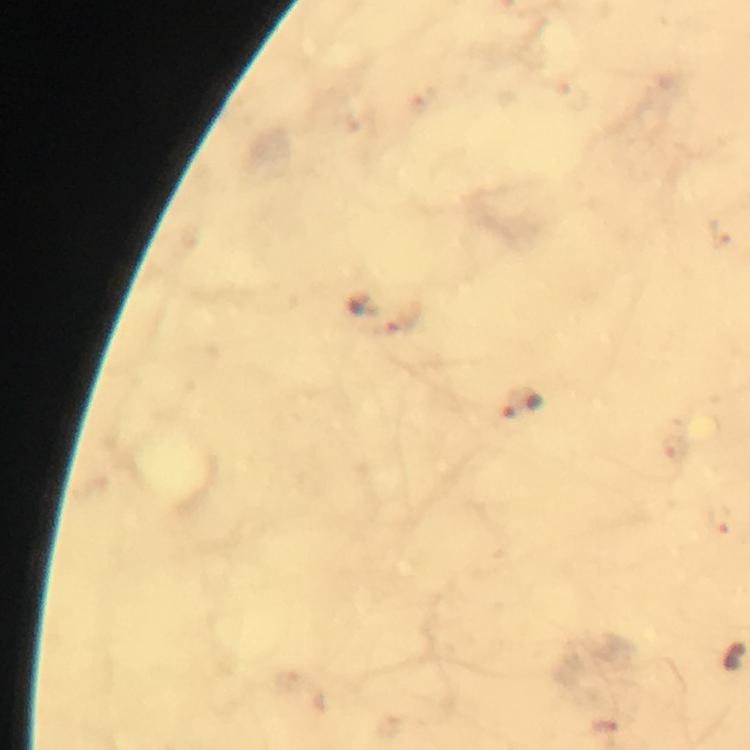
malaria parasite locations = approximate object centers, in pixels from the top-left corner: (x=524, y=400)
immersion oil = used
cropped from = one field of view
preparation = thick blood smear
magnification = 100x
stain = Giemsa
image size = 750×750 pixels
context = from a malaria diagnostic workup
capture = smartphone camera through the microscope